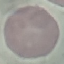

result = no malaria parasites seen
capture = smartphone camera at the microscope eyepiece
stain = Giemsa
preparation = thin smear
image type = cell patch, automatically extracted from a larger field of view and resized to 64 × 64 pixels